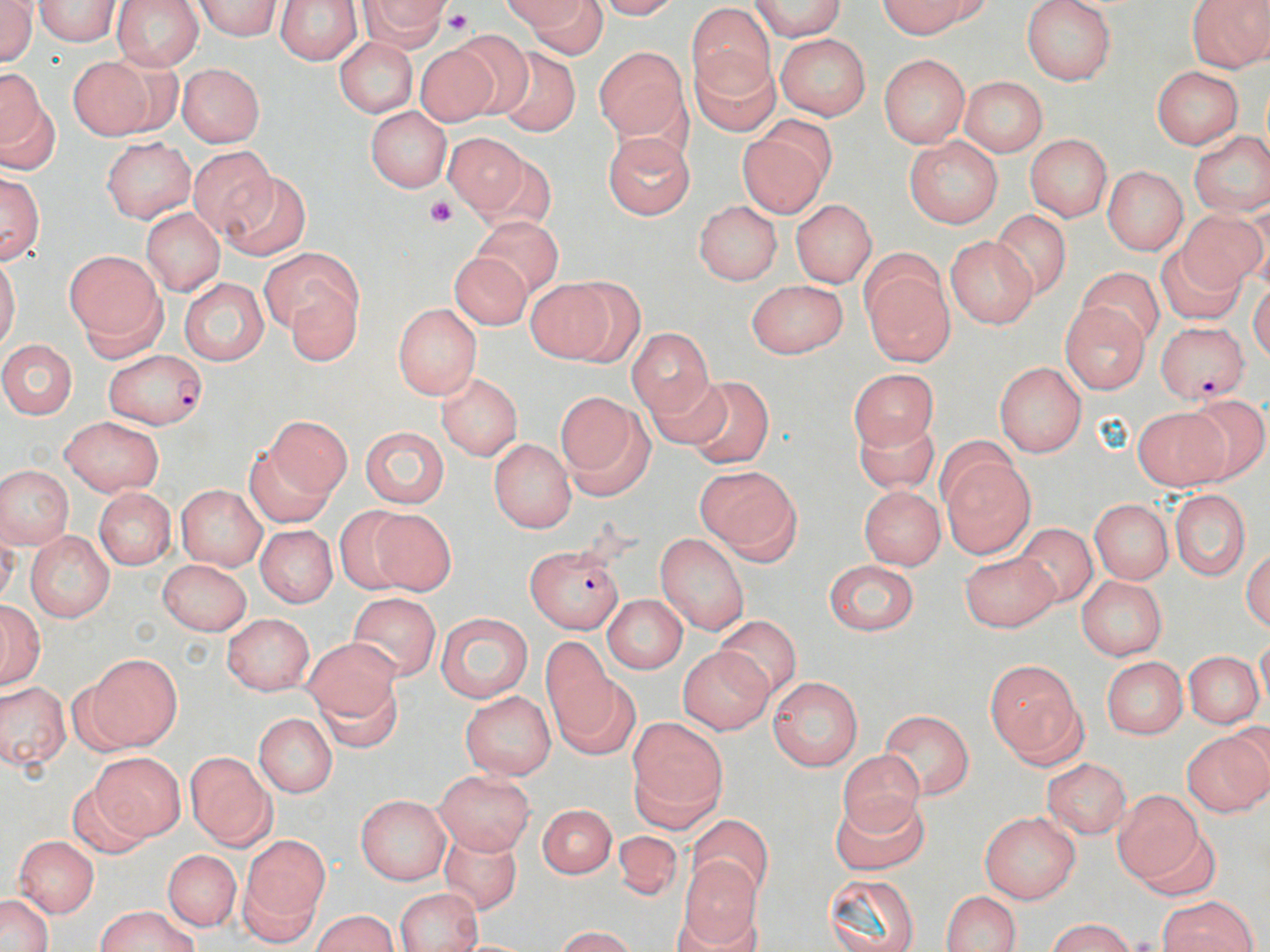

slide_level_diagnosis: Plasmodium falciparum
field_of_view: single
stain: May-Grünwald-Giemsa
modality: optical microscopy
uninfected_red_blood_cell_locations: 'approximate bounding boxes as [x1, y1, x2, y2] in pixels: [0, 0, 38, 69], [110, 0, 206, 71], [357, 0, 453, 59], [745, 0, 849, 39], [872, 0, 1004, 37], [1022, 0, 1117, 84], [1184, 0, 1270, 69], [29, 1, 123, 48], [192, 1, 287, 41], [272, 1, 366, 62], [496, 2, 608, 54], [688, 2, 785, 103], [755, 10, 863, 66], [777, 33, 871, 119], [336, 35, 420, 119], [414, 36, 519, 126], [595, 42, 688, 143], [690, 48, 780, 137], [497, 51, 578, 134], [67, 53, 161, 138], [879, 53, 970, 147], [1153, 63, 1243, 149], [2, 64, 55, 176], [178, 66, 263, 146], [956, 76, 1047, 157], [365, 106, 451, 192], [738, 116, 838, 221], [598, 127, 694, 220], [1187, 127, 1269, 219], [444, 133, 525, 220], [1023, 134, 1114, 220], [900, 135, 1005, 229], [99, 138, 196, 220], [185, 144, 282, 240], [475, 159, 558, 232], [1100, 166, 1188, 257], [0, 168, 47, 269], [218, 173, 310, 264], [692, 198, 782, 286], [788, 198, 875, 286], [141, 203, 223, 297], [1177, 207, 1266, 302], [990, 210, 1068, 298], [474, 217, 563, 294], [945, 235, 1037, 331], [259, 248, 372, 366], [62, 249, 162, 353], [444, 250, 532, 332], [1078, 266, 1162, 343], [863, 268, 962, 371], [178, 277, 271, 361], [527, 277, 643, 362], [745, 278, 844, 358], [391, 300, 484, 396], [1061, 301, 1150, 396], [627, 329, 712, 419], [0, 337, 82, 419], [994, 359, 1087, 457], [643, 369, 733, 457], [433, 370, 525, 464], [850, 372, 937, 454], [694, 377, 771, 466], [554, 388, 654, 499], [1134, 406, 1232, 486], [855, 413, 936, 493], [244, 415, 353, 523], [61, 417, 166, 496], [357, 425, 450, 508], [489, 436, 576, 533], [944, 453, 1033, 558], [1, 463, 72, 546], [696, 464, 804, 566], [177, 484, 268, 566], [92, 487, 174, 570], [1170, 487, 1251, 585], [858, 489, 942, 570], [1091, 497, 1172, 584], [336, 503, 418, 594], [365, 507, 452, 596], [1011, 522, 1104, 606], [254, 525, 336, 609], [24, 532, 112, 621], [655, 532, 751, 638], [958, 544, 1056, 629], [821, 557, 918, 634], [158, 560, 250, 636], [1076, 575, 1165, 662], [346, 590, 440, 684], [601, 593, 688, 674], [1, 597, 45, 690], [436, 611, 533, 702], [224, 613, 315, 698], [714, 616, 802, 704], [541, 631, 625, 753], [303, 634, 400, 728], [677, 641, 773, 734], [76, 651, 182, 752], [1188, 654, 1259, 728], [1100, 657, 1190, 738], [984, 660, 1083, 767], [312, 666, 407, 763], [769, 675, 864, 770], [0, 680, 68, 773], [460, 689, 557, 779], [879, 706, 973, 802], [253, 713, 337, 798], [625, 717, 728, 832], [1181, 728, 1270, 820], [834, 747, 922, 839], [185, 748, 276, 848], [86, 753, 181, 846], [1045, 754, 1133, 838], [431, 770, 533, 855], [1115, 789, 1203, 884], [829, 790, 932, 881], [355, 794, 453, 882], [533, 803, 619, 878], [689, 808, 777, 894], [981, 810, 1082, 902], [437, 826, 523, 919], [614, 826, 682, 905], [235, 831, 330, 941], [12, 834, 95, 916], [164, 846, 240, 928], [681, 853, 759, 948], [823, 876, 922, 952], [391, 888, 481, 952], [0, 889, 56, 952], [938, 890, 1020, 952], [1155, 893, 1261, 952], [94, 907, 202, 952], [307, 909, 403, 952], [1035, 922, 1144, 950], [545, 926, 646, 951]'
preparation: thin blood film
plasmodium_falciparum_infected_red_blood_cell_locations: 'approximate bounding boxes as [x1, y1, x2, y2] in pixels: [1156, 315, 1245, 404], [105, 350, 208, 427], [519, 543, 628, 630]'
magnification: 1000x
image_size: 1270×952 pixels
platelet_locations: 'approximate bounding boxes as [x1, y1, x2, y2] in pixels: [440, 11, 479, 37], [425, 192, 453, 231]'